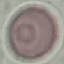

{
  "malaria_status": "uninfected",
  "preparation": "thin blood smear",
  "capture": "smartphone camera at the microscope eyepiece",
  "stain": "Giemsa",
  "image_type": "cell patch, automatically extracted from a larger field of view and resized to 64 × 64 pixels"
}